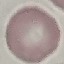 Result: no malaria parasites detected. Automatically extracted cell patch, resized to 64 × 64 pixels. Acquired by smartphone through the microscope eyepiece. Thin blood smear. Giemsa stain.